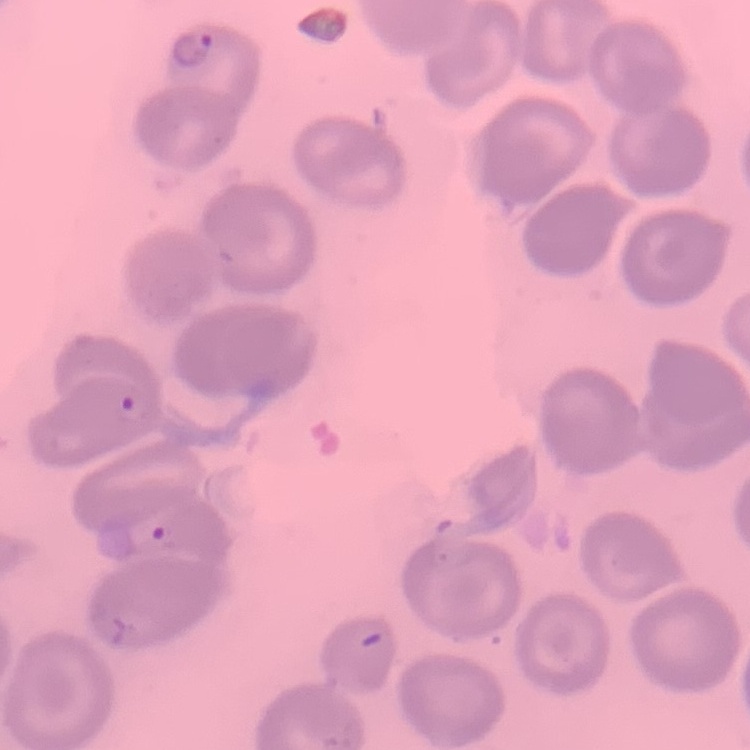

Summary:
  - Erythrocyte morphology: no rouleaux formation
  - Image type: square crop of a larger photomicrograph
  - Stain: Field's or Giemsa
  - Preparation: thin blood film